Locate every Plasmodium falciparum-infected red blood cell.
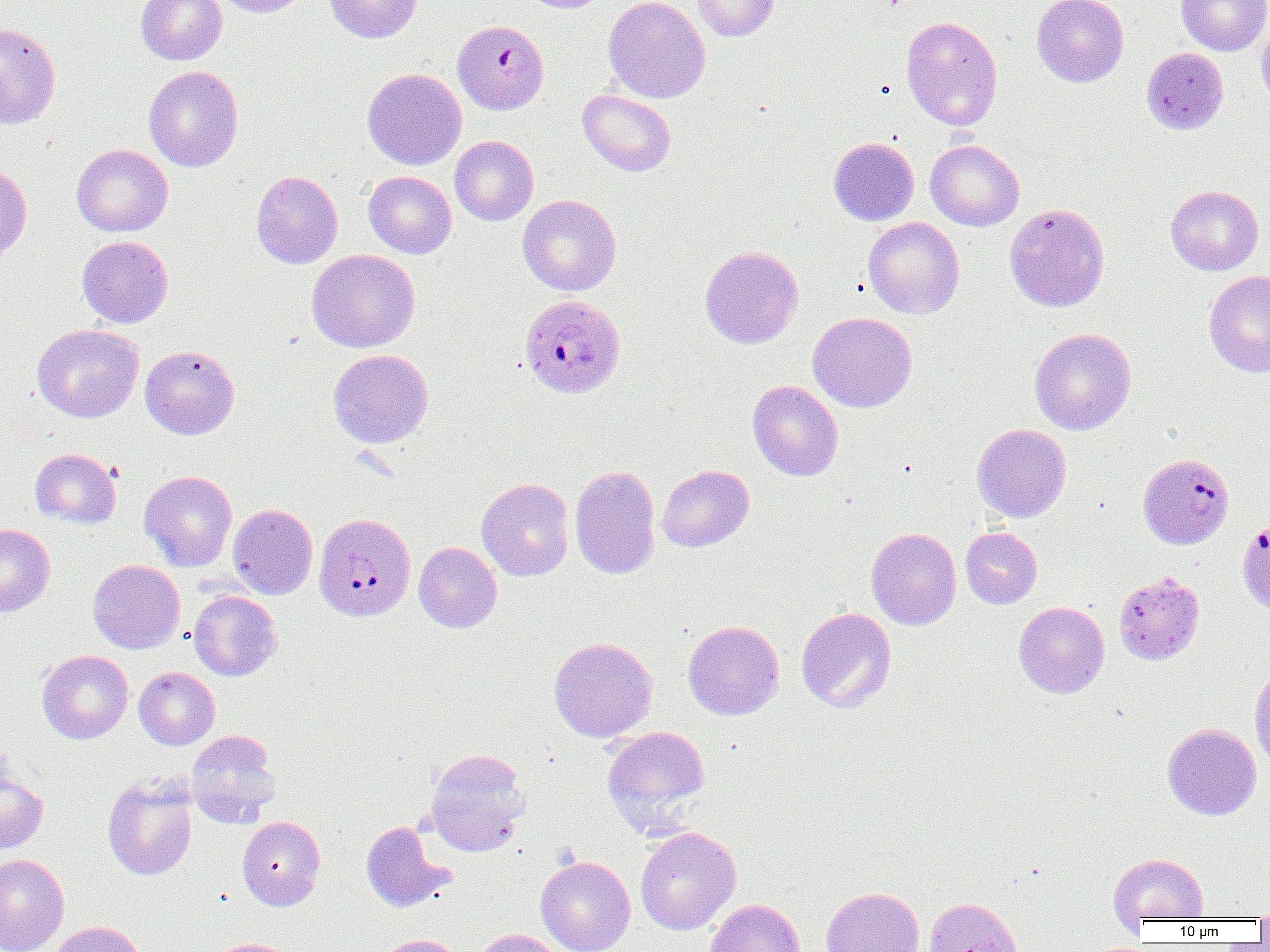

Approximate bounding boxes as (x1, y1, x2, y2) in pixels.
Plasmodium falciparum-infected red blood cells: (454, 23, 549, 115), (519, 293, 626, 399), (1137, 453, 1233, 550), (314, 512, 416, 621), (1237, 517, 1270, 616).

Uninfected red blood cell locations: (136, 0, 227, 65), (213, 0, 310, 18), (325, 0, 424, 43), (517, 0, 612, 13), (603, 0, 711, 103), (691, 0, 779, 42), (1032, 0, 1128, 88), (1176, 0, 1270, 56), (901, 15, 1003, 131), (1256, 16, 1270, 109), (0, 23, 61, 129), (1141, 47, 1229, 135), (143, 66, 243, 171), (361, 67, 467, 170), (577, 89, 676, 176), (450, 136, 538, 225), (829, 136, 919, 226), (925, 139, 1025, 231), (71, 144, 172, 236), (0, 163, 32, 261), (251, 170, 343, 269), (363, 171, 456, 258), (1165, 185, 1264, 276), (518, 194, 621, 296), (1003, 203, 1110, 313), (862, 217, 965, 319), (77, 236, 173, 328), (700, 245, 804, 348), (307, 249, 420, 352), (1204, 270, 1270, 378), (807, 312, 918, 412), (32, 324, 144, 423), (1029, 327, 1137, 435), (140, 344, 240, 440), (328, 349, 434, 448), (747, 380, 844, 481), (972, 424, 1071, 523), (30, 448, 121, 528), (570, 464, 661, 580), (657, 464, 754, 552), (139, 470, 237, 572), (477, 478, 574, 581), (228, 504, 317, 599), (0, 523, 56, 617), (866, 527, 962, 630), (960, 527, 1042, 609), (413, 542, 502, 632), (87, 560, 185, 654), (1113, 571, 1205, 665), (189, 590, 282, 681), (1013, 601, 1110, 698), (796, 607, 897, 712), (682, 620, 784, 721), (548, 636, 658, 742), (36, 650, 133, 744), (1249, 666, 1270, 773), (134, 667, 220, 750), (1162, 723, 1261, 820), (602, 726, 711, 834), (186, 730, 281, 827), (425, 747, 532, 855), (0, 766, 48, 853), (101, 773, 198, 881), (237, 815, 326, 910), (360, 820, 455, 913), (635, 826, 741, 935), (1108, 853, 1209, 923), (0, 854, 69, 952), (535, 855, 635, 952), (821, 886, 925, 952), (924, 897, 1022, 952), (705, 898, 806, 952), (1253, 903, 1270, 928), (47, 920, 147, 952), (469, 928, 566, 952), (375, 934, 465, 952), (206, 937, 297, 952). Slide-level diagnosis: Plasmodium falciparum. Light microscopy. 1000x magnification. One field of a larger specimen. Thin blood smear. Image is 1270×952 pixels.